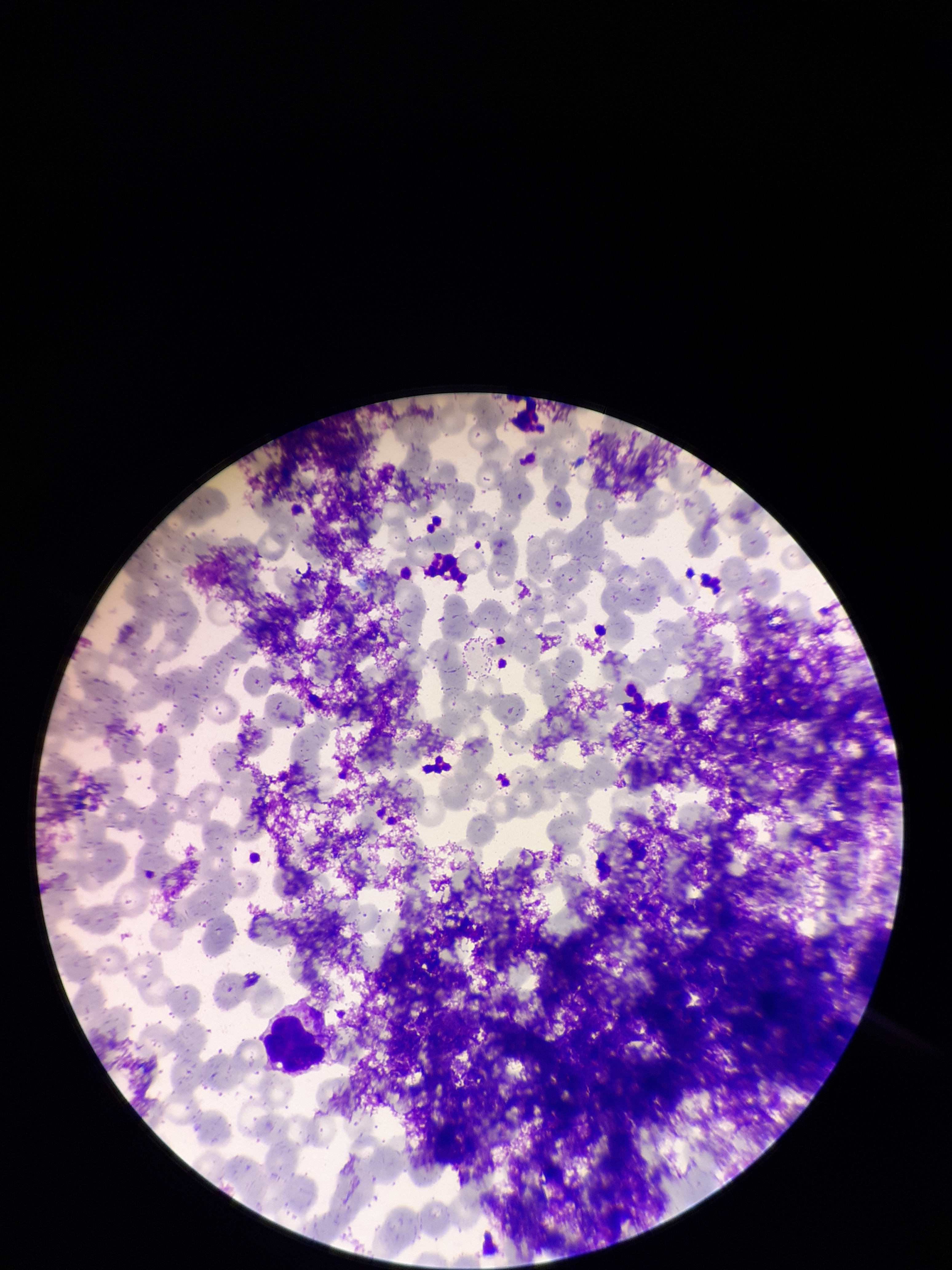
{
  "capture": "smartphone photograph through the microscope eyepiece",
  "parasitized_red_blood_cells": "none identified",
  "red_blood_cell_count": 292,
  "parasitized_red_blood_cell_count": 0,
  "patient_malaria_status": "negative",
  "stain": "Giemsa",
  "image_size": "952×1270 pixels",
  "preparation": "thin smear",
  "field_of_view": "single"
}